Identify the parasite.
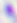

Toxoplasma gondii.

Captured at 400x magnification. Photomicrograph.